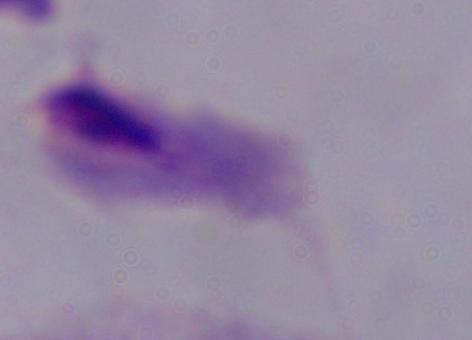
Summary:
  - Modality: photomicrograph
  - Identification: trichomonad
  - Magnification: 1000x